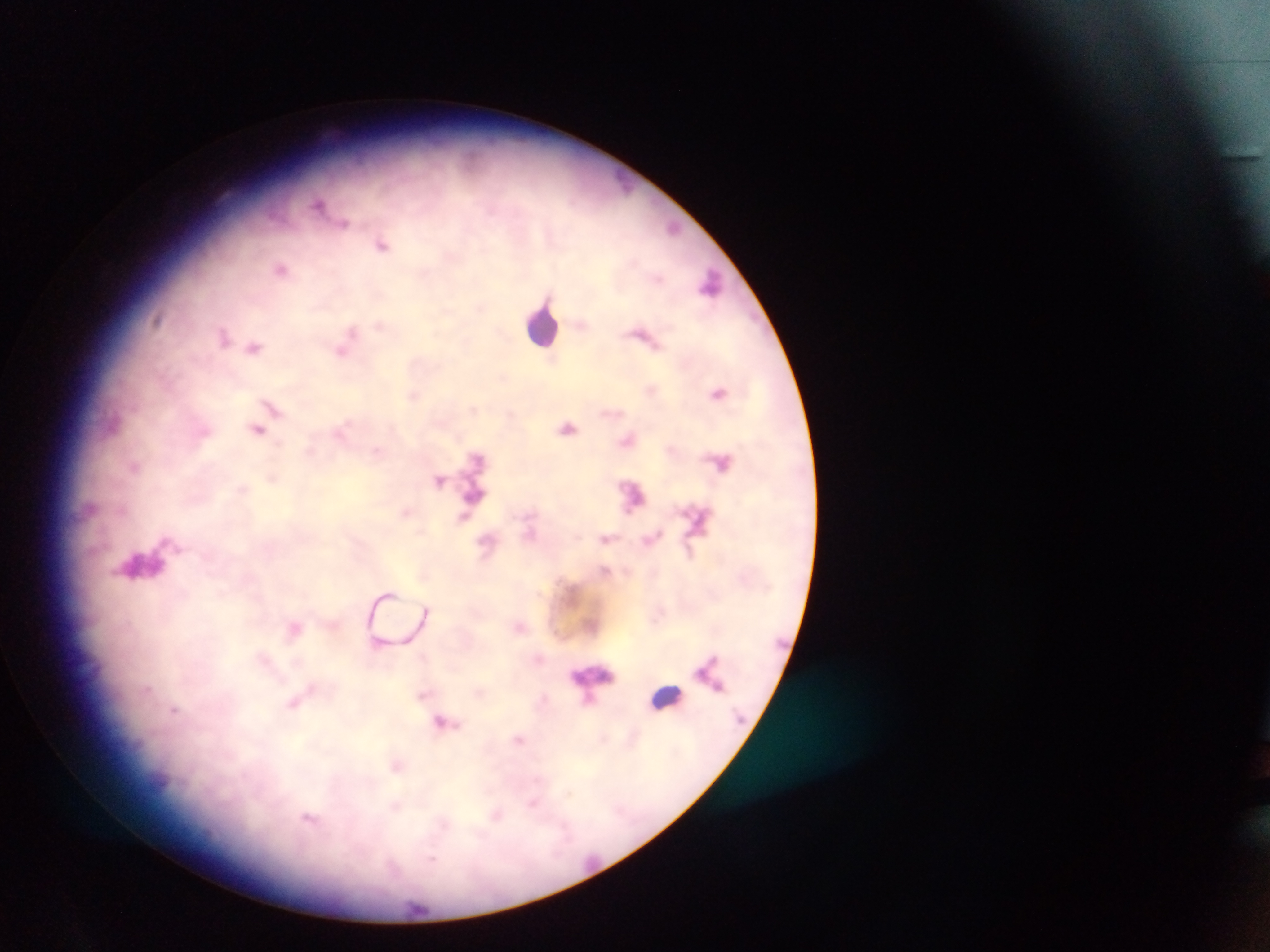
Approximate centers as [x, y] in pixels.
Summary:
  - Leukocyte locations: [711, 284], [542, 324], [138, 563], [593, 679], [666, 697]
  - Malaria parasite locations: [319, 204], [344, 223], [674, 228], [381, 245], [281, 268], [379, 325], [223, 336], [254, 347], [342, 351], [719, 392], [414, 395], [272, 407], [568, 428], [257, 430], [341, 430], [627, 441], [723, 463], [135, 467], [440, 480], [405, 513], [465, 518], [530, 534], [606, 538], [486, 541], [425, 610], [295, 628], [718, 687], [147, 690], [422, 694], [297, 701], [174, 710], [441, 722], [518, 740], [397, 766], [532, 804], [309, 820]
  - Preparation: thick blood smear
  - Field of view: single
  - Image size: 1270×952 pixels
  - Capture: mobile-phone photograph through a microscope
  - Country: Ghana